Assess the morphology of the red blood cells.
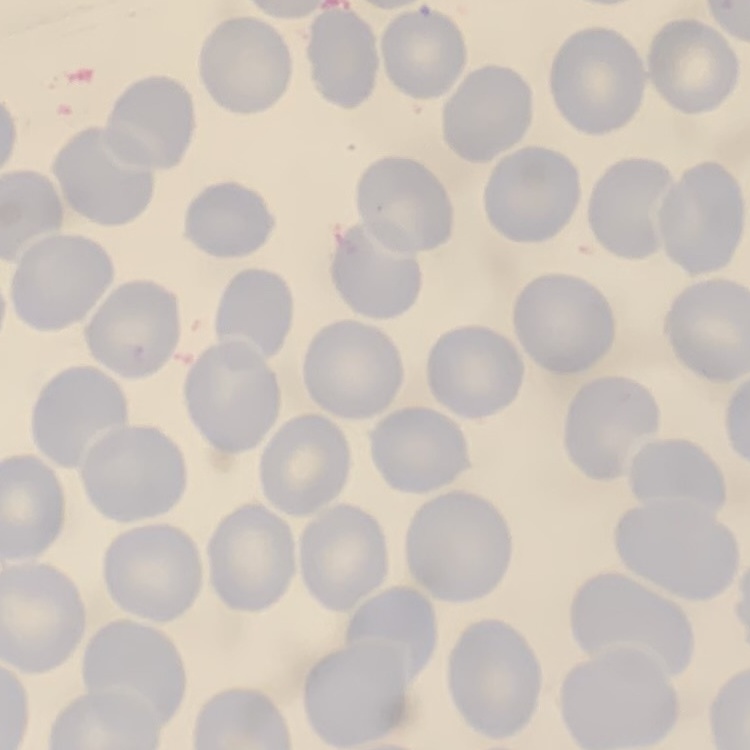

They show no rouleaux formation.

Summary:
  - Preparation: thin blood film
  - Stain: Field's or Giemsa
  - Image type: one tile cut from a larger photomicrograph